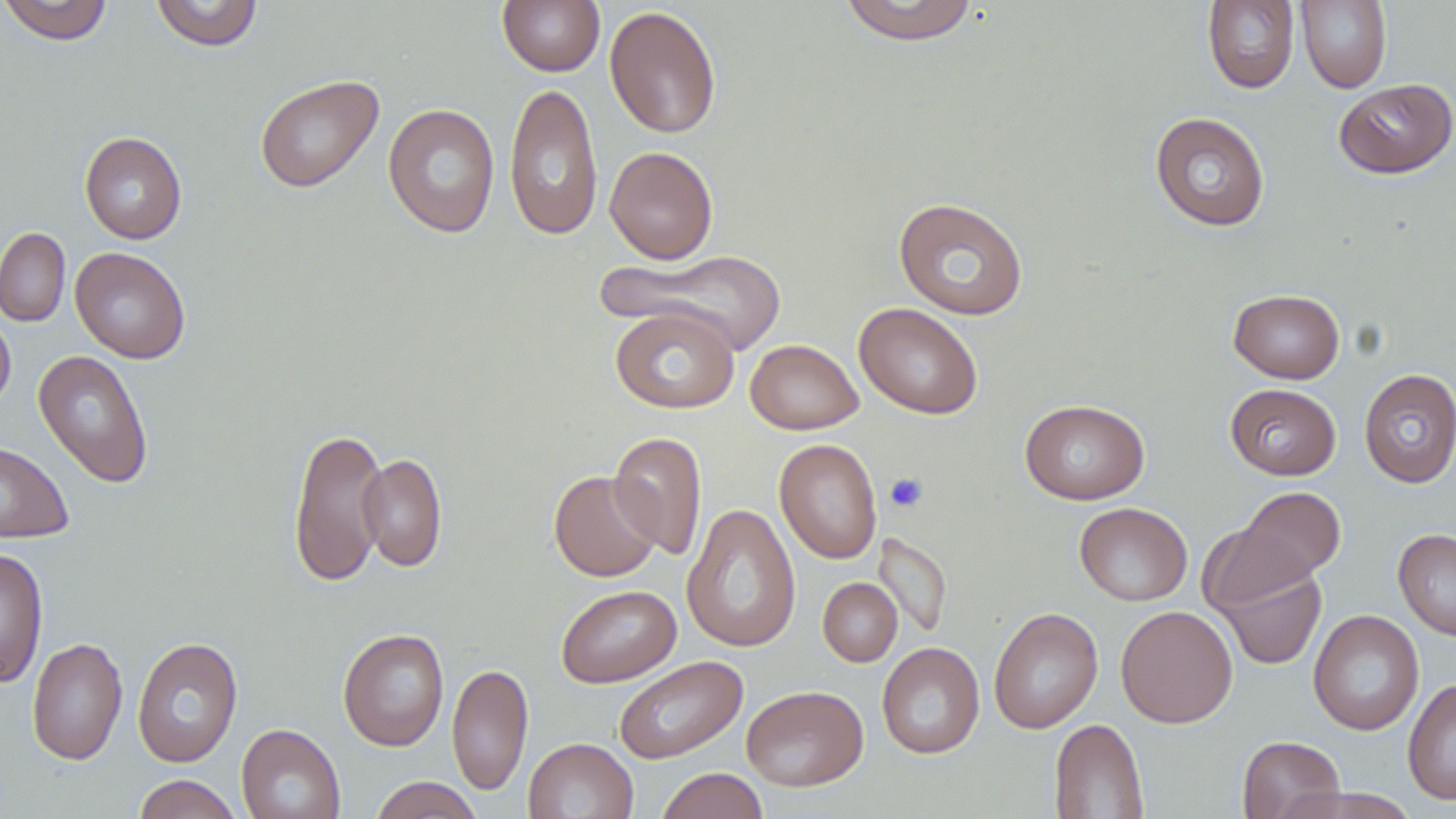

Summary:
  - Coordinate format: approximate bounding boxes as (x1, y1, x2, y2) in pixels
  - Platelet locations: (884, 472, 928, 512)
  - Uninfected red blood cell locations: (0, 0, 114, 45), (150, 0, 264, 51), (497, 0, 605, 76), (838, 0, 980, 44), (1202, 0, 1299, 93), (1295, 1, 1392, 93), (605, 5, 721, 139), (254, 75, 384, 193), (1334, 79, 1455, 179), (504, 81, 603, 242), (383, 103, 500, 238), (1150, 111, 1271, 232), (79, 131, 187, 244), (605, 145, 718, 264), (893, 197, 1029, 320), (0, 227, 71, 327), (70, 246, 191, 363), (606, 250, 788, 356), (1228, 288, 1345, 384), (854, 302, 983, 419), (610, 307, 740, 413), (0, 309, 15, 413), (745, 339, 863, 435), (33, 349, 154, 489), (1358, 369, 1456, 488), (1225, 383, 1341, 480), (1020, 398, 1150, 505), (288, 426, 388, 587), (608, 431, 707, 560), (774, 438, 883, 564), (0, 440, 74, 543), (359, 452, 447, 571), (548, 470, 662, 582), (1232, 486, 1345, 590), (681, 502, 801, 653), (1074, 502, 1192, 606), (1197, 518, 1316, 617), (1393, 528, 1456, 640), (873, 532, 952, 639), (0, 547, 48, 688), (1213, 557, 1328, 670), (818, 577, 902, 666), (556, 584, 681, 688), (1115, 605, 1238, 728), (988, 607, 1103, 734), (1308, 609, 1424, 735), (337, 627, 449, 752), (132, 636, 243, 767), (26, 637, 128, 765), (876, 642, 985, 759), (613, 655, 748, 764), (447, 662, 533, 797), (1403, 677, 1456, 805), (741, 685, 868, 791), (1049, 718, 1149, 818), (236, 723, 345, 819), (1237, 735, 1345, 819), (523, 737, 638, 819), (657, 767, 768, 819), (133, 774, 242, 819), (369, 776, 484, 819)
  - Slide-level diagnosis: negative for blood parasites
  - Image size: 1456×819 pixels
  - Magnification: 1000x
  - Modality: optical microscopy
  - Stain: May-Grünwald-Giemsa
  - Field of view: single
  - Preparation: thin blood film